Mark where cells are.
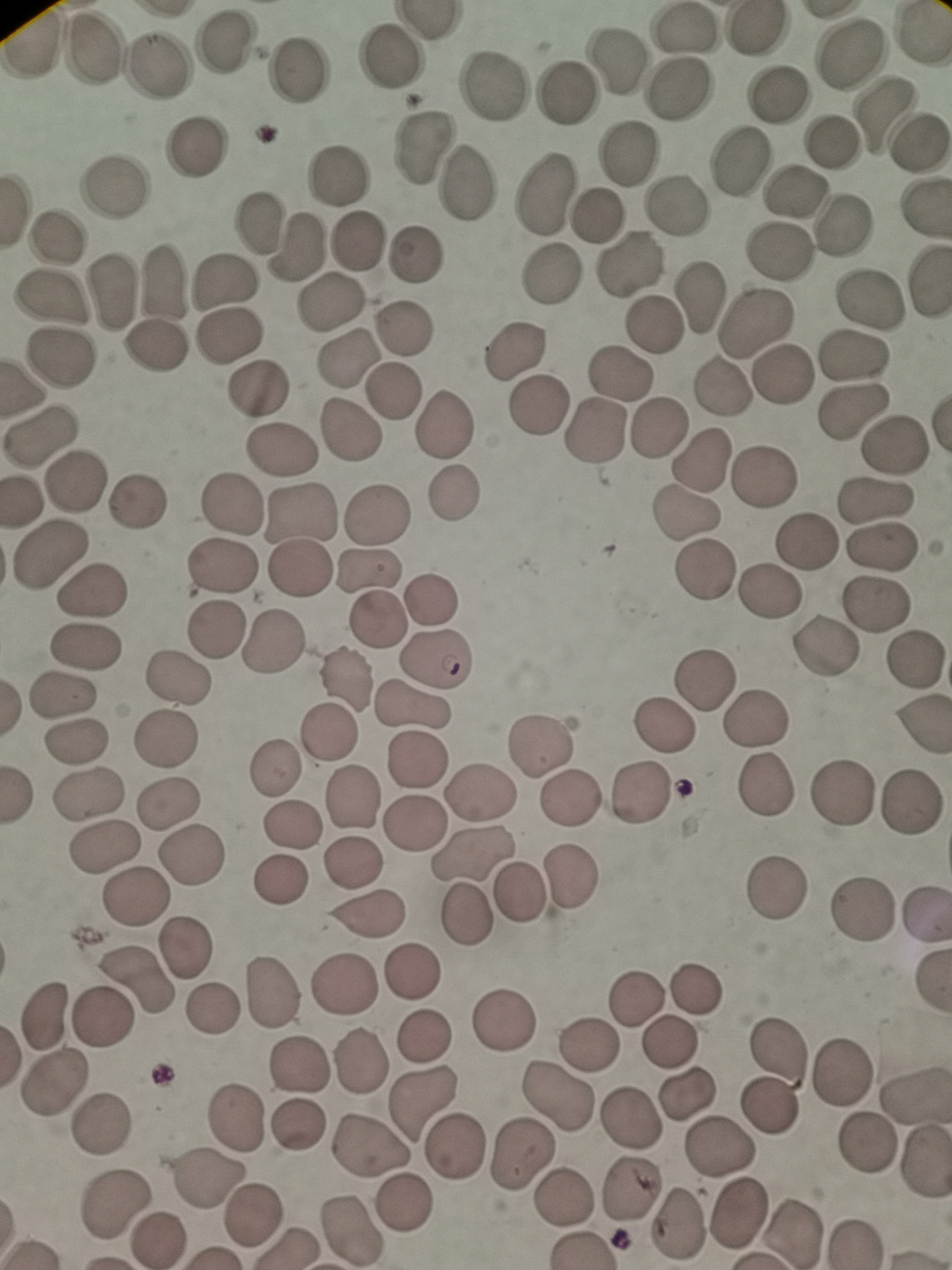

Approximate centers as {x, y} in pixels.
Cells: {685, 27}, {755, 28}, {224, 44}, {90, 49}, {393, 55}, {848, 55}, {614, 59}, {151, 65}, {302, 68}, {492, 86}, {679, 90}, {775, 93}, {564, 94}, {878, 114}, {834, 140}, {918, 143}, {199, 145}, {424, 148}, {627, 154}, {739, 160}, {338, 174}, {466, 183}, {114, 185}, {793, 189}, {544, 196}, {671, 208}, {594, 213}, {262, 222}, {841, 228}, {56, 236}, {356, 239}, {294, 246}, {778, 250}, {416, 255}, {630, 264}, {551, 273}, {158, 281}, {219, 284}, {115, 289}, {54, 297}, {700, 297}, {872, 299}, {331, 302}, {753, 321}, {652, 324}, {400, 327}, {228, 333}, {156, 351}, {514, 352}, {850, 354}, {62, 359}, {350, 361}, {617, 373}, {784, 374}, {256, 387}, {720, 388}, {393, 390}, {537, 406}, {854, 413}, {445, 426}, {659, 428}, {349, 434}, {594, 434}, {45, 436}, {895, 445}, {276, 450}, {702, 460}, {764, 475}, {73, 484}, {453, 495}, {228, 502}, {877, 502}, {135, 504}, {300, 513}, {378, 514}, {687, 520}, {806, 544}, {881, 546}, {52, 559}, {222, 565}, {295, 569}, {703, 570}, {369, 573}, {93, 588}, {433, 595}, {770, 595}, {882, 603}, {378, 620}, {218, 632}, {272, 644}, {87, 645}, {823, 649}, {437, 657}, {915, 660}, {343, 678}, {710, 678}, {178, 680}, {59, 693}, {412, 708}, {754, 721}, {660, 728}, {329, 734}, {77, 737}, {165, 740}, {538, 747}, {416, 760}, {275, 764}, {769, 785}, {88, 791}, {843, 791}, {477, 794}, {642, 795}, {569, 796}, {171, 798}, {350, 798}, {912, 801}, {408, 823}, {290, 824}, {106, 846}, {472, 854}, {189, 856}, {350, 863}, {570, 871}, {277, 879}, {774, 887}, {518, 891}, {136, 898}, {865, 904}, {924, 911}, {366, 913}, {465, 913}, {186, 947}, {411, 972}, {135, 981}, {344, 983}, {695, 987}, {269, 992}, {639, 997}, {211, 1009}, {46, 1018}, {506, 1018}, {102, 1019}, {424, 1035}, {588, 1040}, {671, 1040}, {778, 1043}, {359, 1061}, {298, 1067}, {840, 1068}, {51, 1081}, {687, 1091}, {915, 1091}, {560, 1098}, {425, 1100}, {772, 1106}, {627, 1117}, {234, 1121}, {100, 1123}, {296, 1125}, {368, 1145}, {865, 1145}, {717, 1146}, {456, 1147}, {520, 1154}, {923, 1164}, {207, 1181}, {635, 1192}, {563, 1198}, {115, 1199}, {404, 1203}, {737, 1215}, {253, 1217}, {675, 1225}, {348, 1229}, {794, 1232}, {159, 1239}.

field_of_view: single
stain: Giemsa
capture: smartphone through the microscope eyepiece
image_size: 952×1270 pixels
preparation: thin smear